Name the blood parasite species.
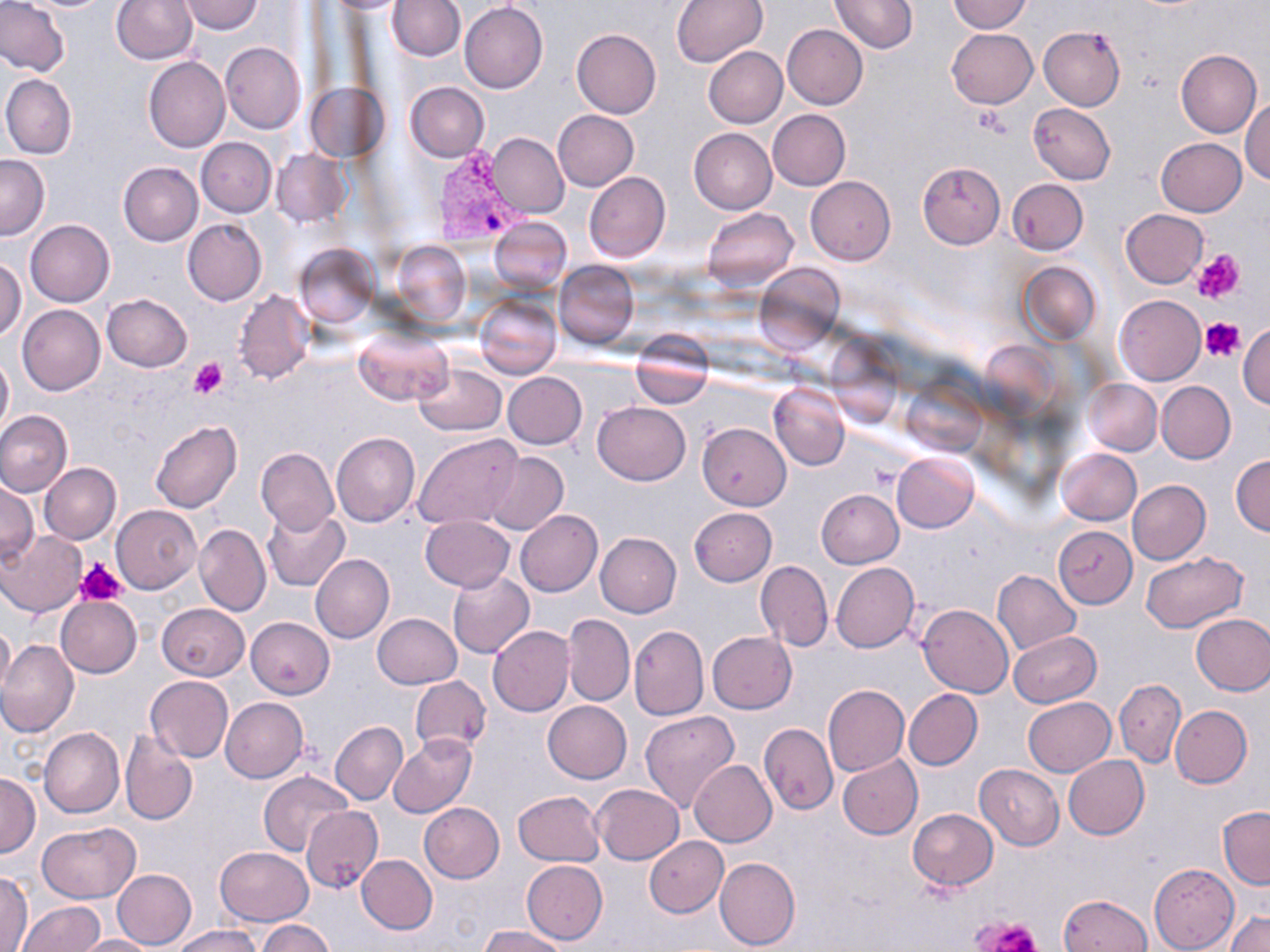

Plasmodium vivax.

Summary:
  - Coordinate format: approximate bounding boxes as [x1, y1, x2, y2] in pixels
  - Plasmodium vivax-infected red blood cell locations: [435, 147, 531, 248]
  - Platelet locations: [973, 107, 1011, 139], [1193, 249, 1244, 303], [1200, 318, 1245, 362], [190, 357, 227, 399], [76, 558, 129, 605], [978, 916, 1040, 952]
  - Uninfected red blood cell locations: [0, 0, 70, 77], [178, 0, 264, 34], [327, 0, 410, 15], [387, 0, 464, 61], [671, 0, 768, 67], [828, 0, 917, 54], [946, 0, 1032, 33], [111, 1, 197, 66], [460, 1, 548, 93], [783, 23, 867, 110], [1039, 25, 1125, 111], [947, 28, 1037, 107], [571, 29, 661, 119], [221, 43, 306, 133], [703, 47, 787, 129], [1176, 49, 1261, 137], [143, 57, 230, 152], [2, 74, 76, 159], [406, 82, 490, 163], [305, 85, 386, 162], [1241, 97, 1270, 184], [1028, 103, 1116, 185], [552, 110, 639, 191], [767, 110, 850, 191], [690, 128, 777, 214], [489, 133, 568, 217], [196, 138, 277, 216], [1156, 138, 1247, 217], [272, 148, 351, 227], [0, 154, 50, 240], [118, 161, 203, 245], [918, 161, 1006, 249], [584, 172, 670, 263], [805, 176, 895, 265], [1007, 179, 1087, 255], [702, 208, 799, 291], [1120, 209, 1208, 288], [488, 215, 571, 295], [25, 219, 114, 307], [182, 219, 267, 305], [392, 243, 471, 327], [295, 244, 378, 327], [0, 258, 26, 340], [553, 261, 639, 349], [1018, 261, 1101, 344], [754, 263, 844, 349], [234, 291, 313, 384], [101, 293, 192, 371], [474, 295, 562, 379], [1113, 295, 1206, 385], [18, 305, 105, 394], [1238, 322, 1269, 406], [354, 327, 452, 407], [629, 338, 714, 407], [0, 352, 12, 437], [412, 363, 507, 436], [502, 372, 586, 448], [1083, 378, 1161, 455], [1156, 381, 1236, 464], [902, 382, 984, 454], [769, 383, 850, 470], [592, 402, 690, 485], [0, 410, 73, 497], [150, 421, 242, 512], [697, 423, 791, 510], [332, 433, 420, 528], [414, 434, 524, 531], [256, 446, 338, 534], [1058, 448, 1141, 525], [486, 452, 568, 535], [893, 452, 979, 532], [1230, 455, 1270, 536], [40, 463, 120, 545], [1127, 480, 1210, 564], [1, 481, 39, 564], [816, 489, 904, 569], [111, 505, 201, 593], [261, 507, 349, 591], [689, 507, 777, 587], [515, 509, 603, 596], [419, 516, 513, 592], [194, 524, 270, 616], [1053, 525, 1138, 609], [2, 531, 86, 616], [595, 533, 681, 618], [1141, 553, 1248, 634], [311, 554, 394, 644], [756, 560, 833, 652], [831, 562, 921, 653], [992, 569, 1081, 655], [447, 570, 534, 659], [55, 596, 142, 679], [156, 603, 249, 681], [918, 605, 1014, 697], [373, 613, 462, 688], [562, 613, 634, 706], [1190, 614, 1270, 695], [246, 617, 334, 699], [0, 621, 14, 693], [488, 625, 574, 718], [629, 625, 708, 720], [1010, 631, 1100, 707], [707, 632, 797, 713], [0, 641, 79, 738], [146, 675, 233, 763], [410, 675, 490, 754], [1114, 679, 1185, 767], [822, 685, 909, 776], [904, 689, 983, 770], [220, 697, 307, 783], [1022, 697, 1115, 776], [543, 700, 632, 783], [1170, 704, 1252, 788], [640, 710, 740, 814], [330, 721, 408, 805], [759, 723, 837, 815], [39, 727, 124, 818], [121, 729, 197, 825], [388, 733, 477, 817], [838, 754, 923, 841], [1064, 755, 1149, 839], [690, 760, 776, 847], [975, 764, 1064, 849], [260, 771, 353, 857], [1, 774, 40, 857], [593, 783, 684, 864], [512, 790, 604, 866], [419, 803, 504, 882], [302, 806, 383, 891], [1218, 806, 1270, 890], [908, 809, 998, 889], [38, 822, 140, 903], [644, 836, 727, 917], [215, 846, 313, 924], [357, 854, 437, 934], [715, 855, 800, 951], [521, 859, 608, 944], [1149, 863, 1238, 951], [112, 869, 196, 950], [0, 870, 33, 952], [1059, 894, 1152, 952], [15, 901, 104, 951], [1226, 912, 1270, 952], [259, 919, 336, 952], [172, 925, 260, 951], [479, 926, 568, 951], [75, 935, 156, 952]
  - Stain: May-Grünwald-Giemsa
  - Modality: light microscopy
  - Field of view: one of a larger specimen
  - Magnification: 1000x
  - Image size: 1270×952 pixels
  - Preparation: thin blood film